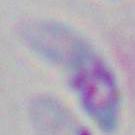
Photomicrograph. Toxoplasma gondii is seen. Captured at 1000x magnification.